Assess the morphology of the erythrocytes.
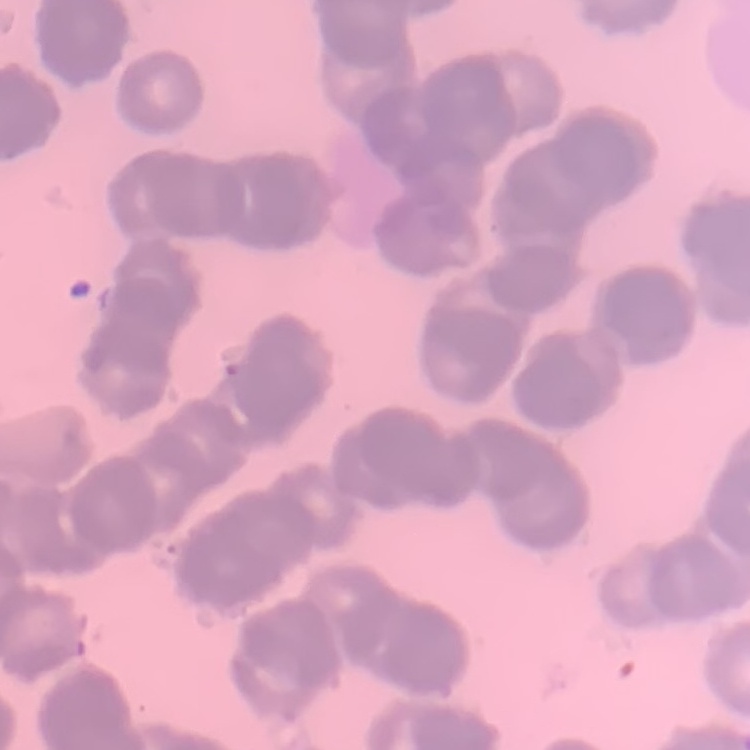
Rouleaux formation.

Summary:
  - Preparation: thin peripheral smear
  - Stain: Field's or Giemsa
  - Image type: one tile cut from a larger photomicrograph